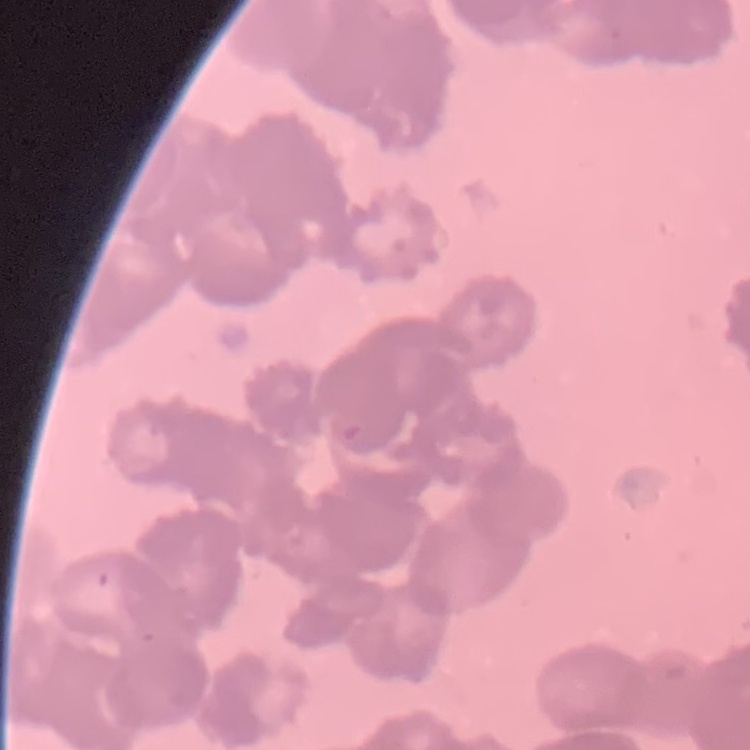

The red blood cells exhibit rouleaux formation. Field's or Giemsa stain. One tile cut from a larger photomicrograph. Thin blood film.